Locate every leukocyte (white blood cell).
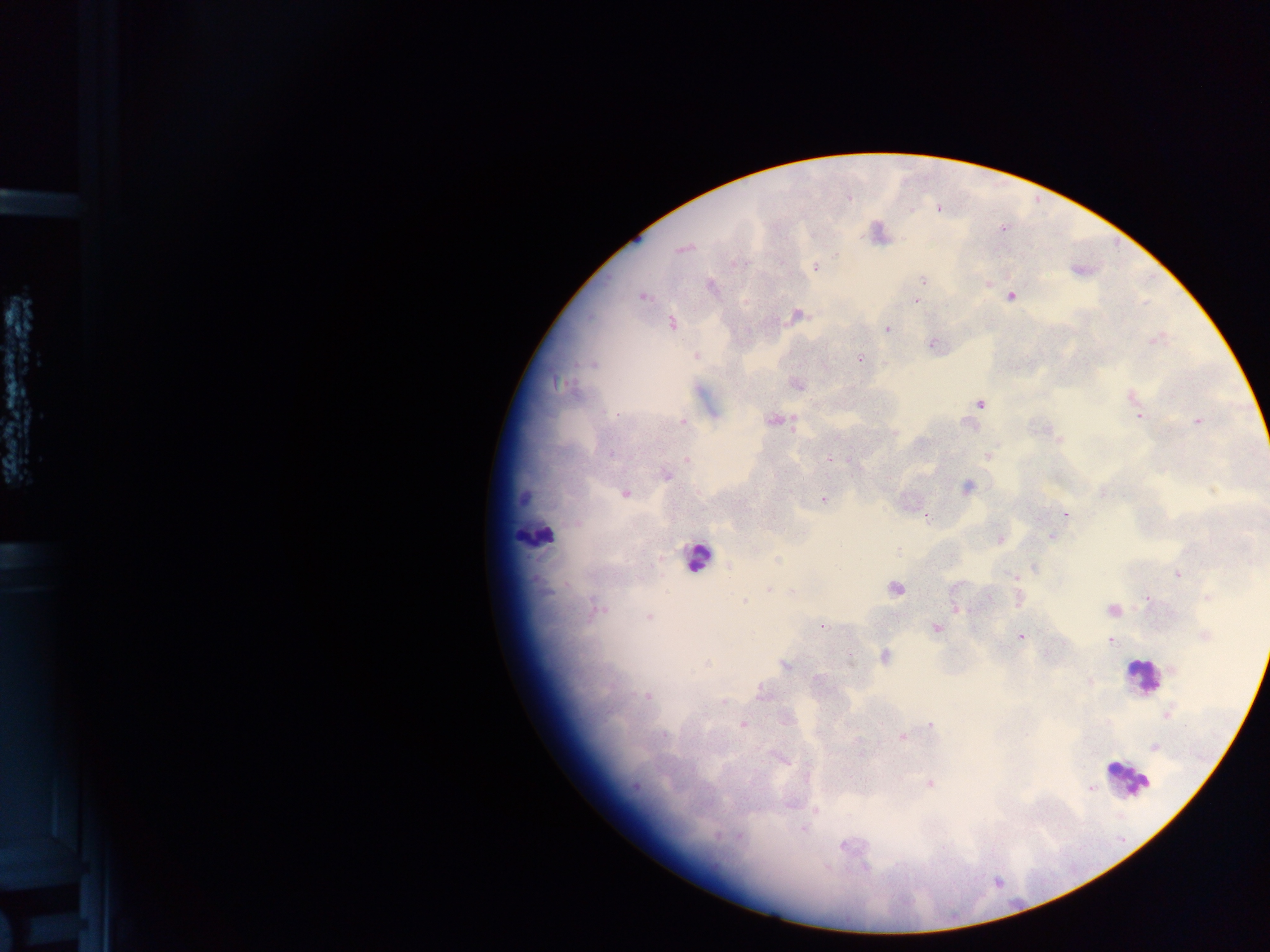
Approximate centers as {x, y} in pixels.
Leukocytes: {534, 534}, {696, 557}, {1142, 677}, {1128, 780}.

Malaria parasite locations: {938, 209}, {911, 210}, {1002, 228}, {682, 249}, {816, 268}, {923, 279}, {988, 283}, {710, 285}, {1012, 296}, {643, 297}, {916, 300}, {798, 316}, {672, 323}, {886, 329}, {1156, 340}, {932, 344}, {696, 356}, {860, 358}, {592, 365}, {557, 383}, {796, 385}, {1132, 397}, {980, 404}, {617, 414}, {1140, 416}, {774, 420}, {1197, 421}, {683, 422}, {895, 433}, {1058, 437}, {610, 454}, {988, 455}, {830, 459}, {687, 460}, {665, 476}, {967, 487}, {625, 494}, {1102, 494}, {824, 500}, {1065, 514}, {1051, 537}, {1000, 539}, {897, 550}, {778, 560}, {729, 566}, {1035, 568}, {1178, 575}, {1014, 576}, {956, 587}, {894, 589}, {768, 590}, {1208, 597}, {988, 598}, {1148, 598}, {1019, 599}, {745, 601}, {955, 609}, {597, 610}, {1112, 610}, {648, 616}, {821, 626}, {936, 628}, {1205, 636}, {1021, 637}, {1111, 641}, {1046, 654}, {884, 656}, {785, 665}, {1173, 669}, {818, 679}, {1090, 682}, {762, 692}, {647, 696}, {724, 702}, {1167, 713}, {783, 720}, {742, 724}, {931, 725}, {665, 734}, {901, 737}, {1154, 747}, {930, 783}, {636, 786}, {1090, 789}, {816, 810}, {803, 828}, {843, 845}. Mobile-phone photograph taken through the microscope. Thick blood smear. Image is 1270×952 pixels. One field of view. Collected in Ghana.